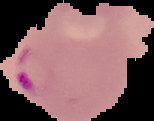
malaria status = parasitized
image size = 154×121 pixels
preparation = thin blood film
image type = segmented cell region with the area outside set to black